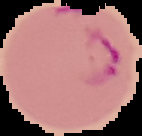

Image is 142×136 pixels. From a thin blood film. Cell region segmented out of the field of view; the surrounding area is masked to black. Malaria status: parasitized.